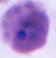 Micrograph. A Plasmodium parasite is shown. 400x or 1000x magnification.